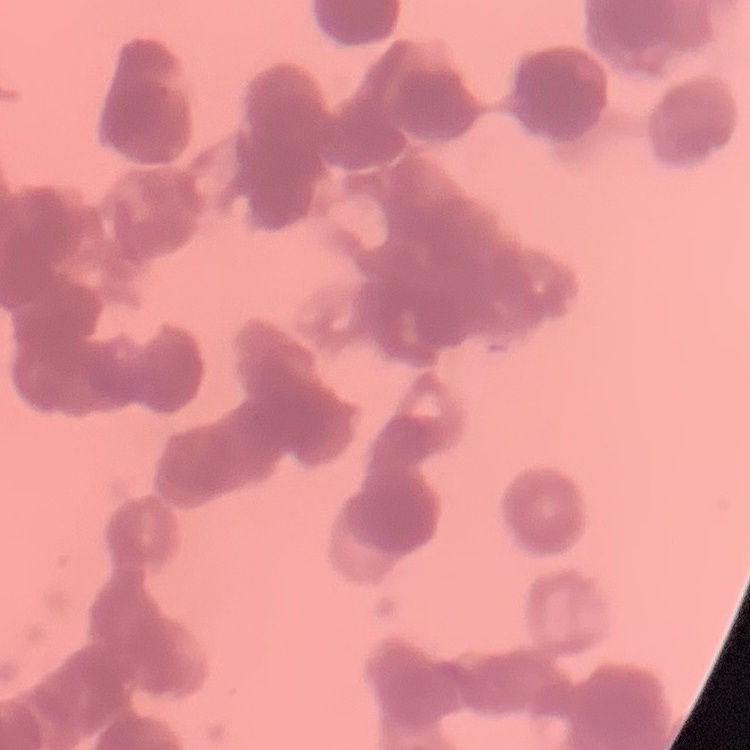
erythrocyte morphology = rouleaux formation
image type = one tile cut from a larger photomicrograph
stain = Field's or Giemsa
preparation = thin blood film